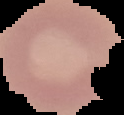

The area outside the segmented cell region is set to black. Image is 124×115 pixels. Malaria status: uninfected. From a thin blood smear.